Look for parasitized red blood cells.
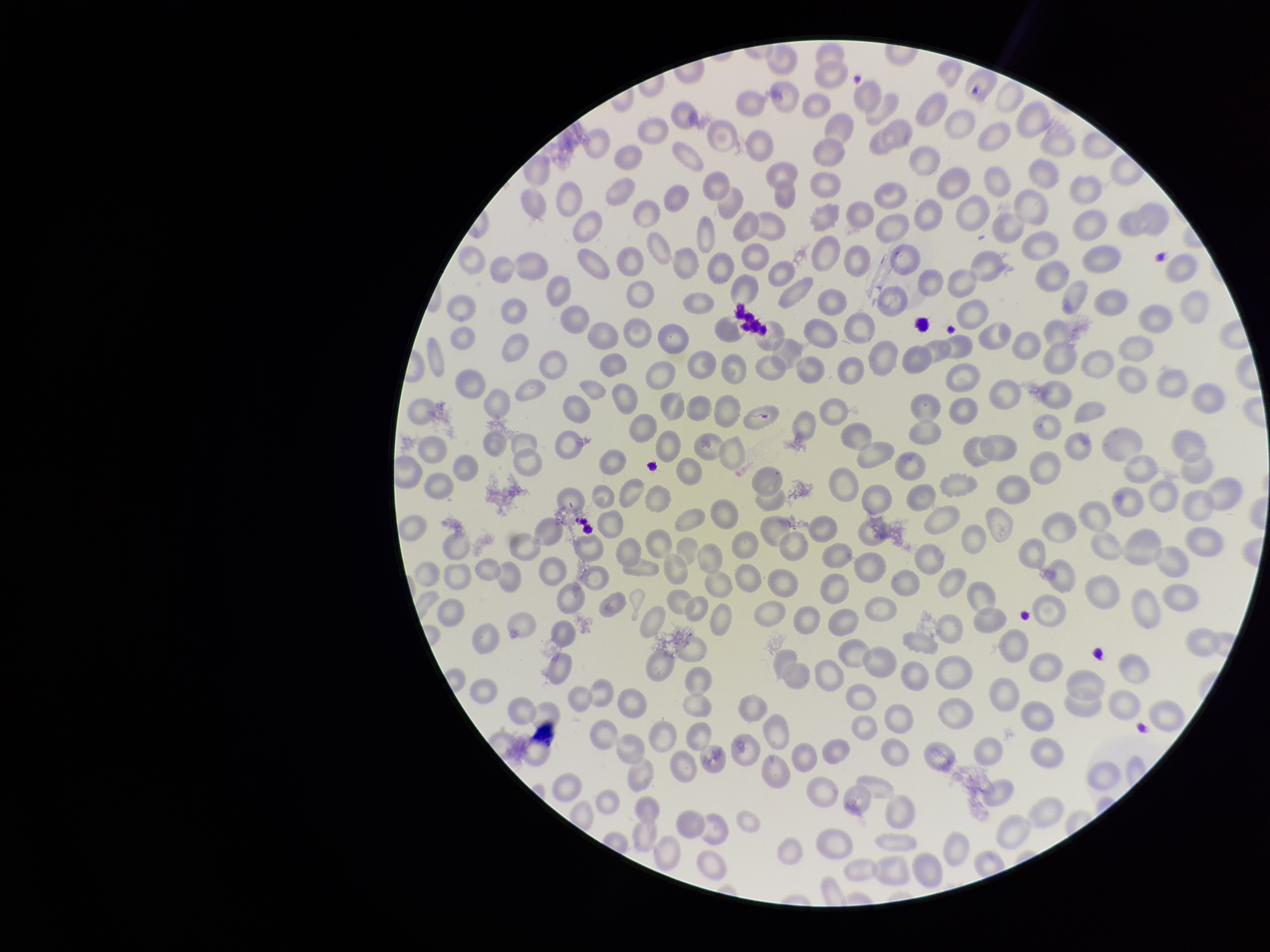

None seen.

Summary:
  - Red blood cell count: 280
  - Capture: smartphone photograph through the microscope eyepiece
  - Parasitized red blood cell count: 0
  - Preparation: thin
  - Image size: 1270×952 pixels
  - Field of view: one from this slide
  - Stain: Giemsa
  - Patient malaria status: negative